Classify this cell by malaria status.
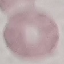
Uninfected.

Acquired by smartphone through the microscope eyepiece. Thin blood smear. Cell patch, automatically extracted from a larger field of view and resized to 64 × 64 pixels. Giemsa stain.